Report the malaria status of this cell.
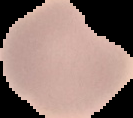

Uninfected.

Summary:
  - Image type: segmented cell region with the area outside set to black
  - Image size: 133×118 pixels
  - Preparation: thin blood smear